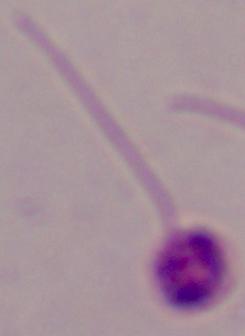 Photomicrograph. 1000x magnification. A Leishmania parasite is seen.